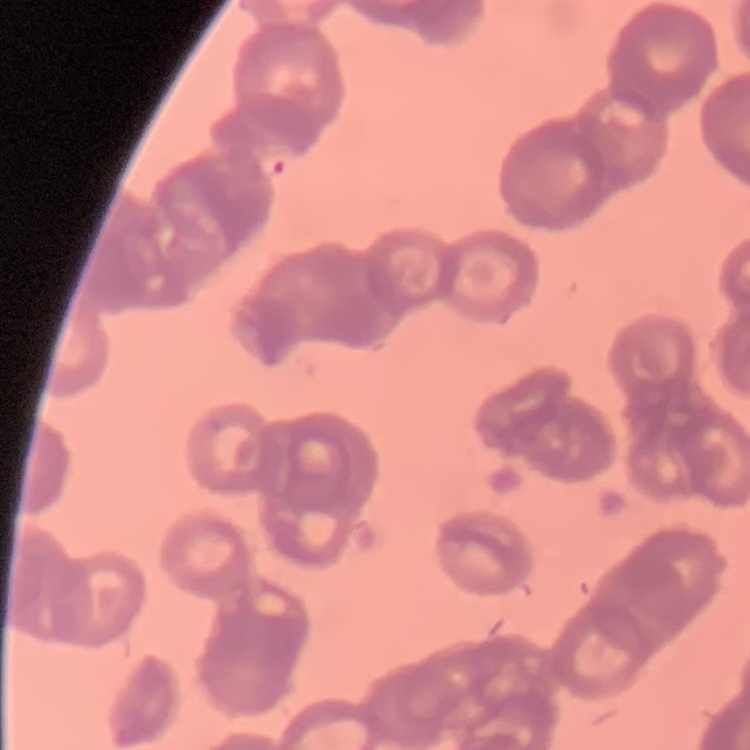
erythrocyte morphology = rouleaux formation
image type = square crop of a larger photomicrograph
stain = Field's or Giemsa
preparation = thin peripheral smear